Identify the preparation type.
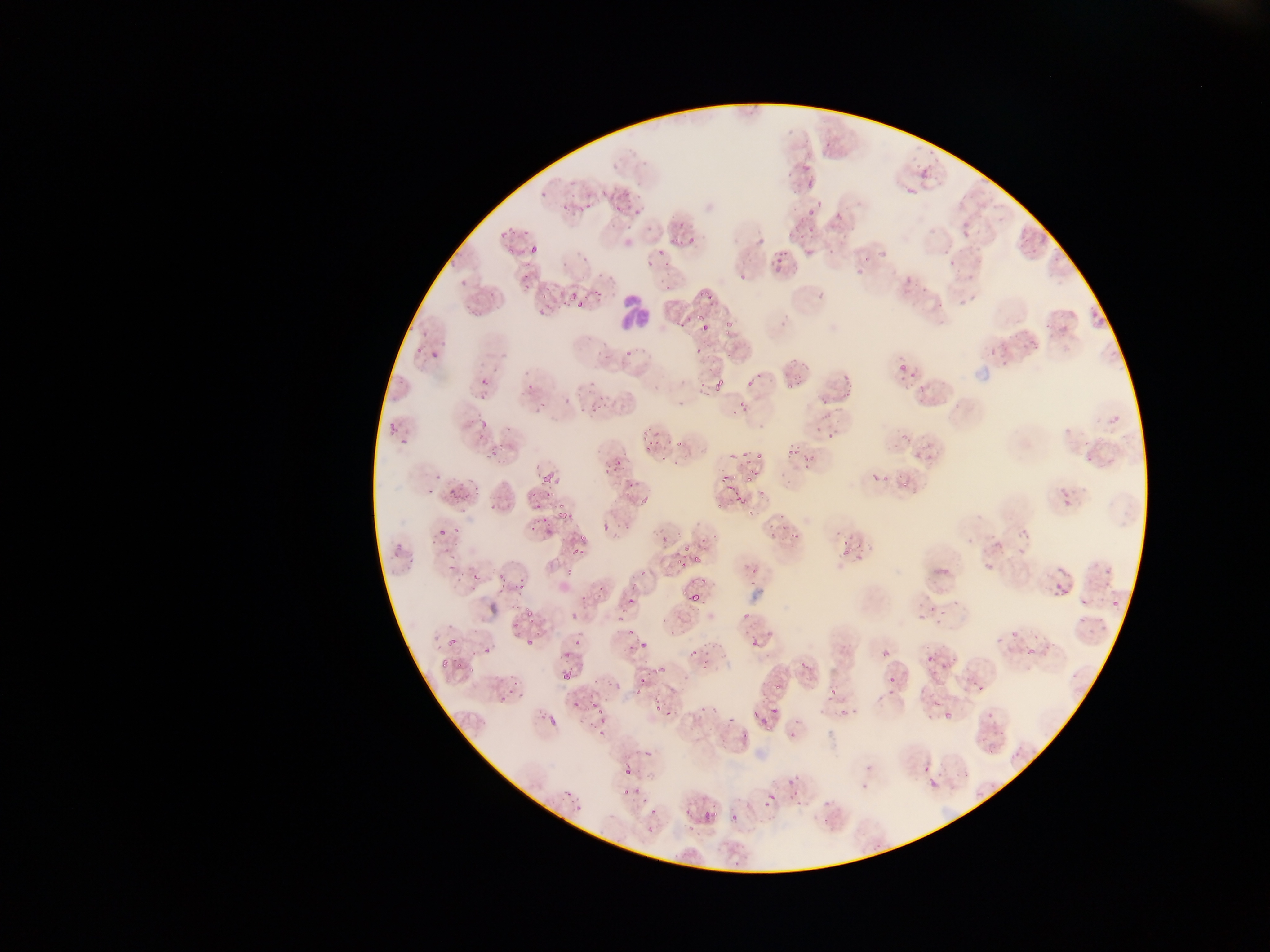
Thin blood smear.

field_of_view: single
leukocyte_locations: 'approximate bounding boxes as {left, top, right, bottom} in pixels: {611, 271, 653, 331}'
image_size: 1270×952 pixels
country: Ghana
malaria_parasite_locations: 'approximate bounding boxes as {left, top, right, bottom} in pixels: {786, 118, 800, 136}, {798, 144, 818, 163}, {913, 145, 932, 162}, {920, 165, 934, 175}, {795, 174, 812, 191}, {908, 183, 918, 193}, {538, 190, 548, 206}, {601, 190, 611, 198}, {611, 192, 641, 217}, {802, 197, 822, 229}, {566, 198, 586, 211}, {504, 216, 521, 241}, {823, 216, 852, 241}, {665, 222, 682, 245}, {957, 225, 971, 239}, {785, 227, 804, 239}, {680, 234, 689, 244}, {620, 235, 631, 249}, {524, 239, 541, 254}, {748, 239, 762, 253}, {859, 244, 882, 269}, {645, 245, 668, 260}, {771, 245, 788, 272}, {505, 247, 517, 258}, {945, 256, 955, 270}, {734, 267, 749, 282}, {514, 269, 535, 289}, {957, 272, 974, 283}, {903, 273, 913, 290}, {455, 279, 472, 290}, {697, 285, 712, 298}, {537, 288, 558, 312}, {957, 289, 984, 312}, {812, 291, 832, 307}, {566, 292, 592, 306}, {462, 302, 483, 324}, {719, 305, 737, 330}, {1084, 311, 1105, 331}, {672, 313, 689, 331}, {700, 322, 710, 333}, {404, 331, 438, 358}, {1022, 335, 1037, 349}, {588, 337, 611, 362}, {689, 341, 705, 358}, {621, 343, 642, 358}, {982, 343, 1002, 354}, {426, 345, 447, 362}, {787, 355, 800, 366}, {999, 360, 1009, 371}, {899, 362, 922, 381}, {744, 365, 763, 392}, {838, 366, 856, 397}, {787, 373, 799, 392}, {476, 375, 502, 398}, {516, 377, 536, 397}, {709, 382, 724, 393}, {584, 387, 612, 416}, {826, 391, 843, 407}, {677, 393, 699, 408}, {732, 397, 750, 416}, {533, 398, 553, 415}, {474, 408, 492, 429}, {1110, 411, 1122, 422}, {385, 419, 401, 441}, {818, 420, 844, 441}, {896, 428, 906, 445}, {642, 430, 661, 453}, {670, 438, 681, 456}, {913, 443, 934, 458}, {488, 446, 496, 455}, {788, 446, 797, 456}, {748, 453, 763, 462}, {800, 454, 813, 469}, {1084, 454, 1097, 469}, {605, 459, 623, 479}, {432, 464, 445, 482}, {541, 468, 556, 486}, {867, 470, 882, 488}, {721, 472, 732, 489}, {457, 475, 483, 500}, {746, 475, 759, 486}, {624, 476, 641, 489}, {884, 476, 889, 486}, {900, 477, 906, 485}, {1059, 481, 1077, 513}, {425, 484, 435, 497}, {444, 489, 455, 503}, {736, 491, 746, 503}, {487, 492, 506, 517}, {635, 495, 651, 508}, {715, 501, 725, 512}, {556, 504, 568, 518}, {532, 505, 550, 530}, {744, 507, 757, 518}, {435, 516, 457, 545}, {602, 517, 615, 536}, {784, 519, 800, 533}, {963, 528, 982, 543}, {1017, 528, 1034, 555}, {654, 530, 675, 555}, {699, 531, 710, 542}, {716, 532, 722, 543}, {841, 533, 859, 559}, {579, 534, 586, 544}, {389, 541, 410, 562}, {567, 545, 574, 555}, {674, 552, 685, 571}, {692, 555, 700, 564}, {448, 557, 462, 578}, {979, 557, 996, 578}, {743, 558, 762, 579}, {1102, 563, 1114, 580}, {560, 564, 578, 581}, {932, 564, 950, 582}, {638, 568, 649, 582}, {469, 569, 482, 584}, {493, 572, 508, 593}, {1049, 575, 1069, 599}, {511, 579, 527, 597}, {1076, 583, 1098, 609}, {591, 584, 605, 599}, {628, 589, 635, 604}, {689, 593, 697, 601}, {1111, 595, 1124, 608}, {920, 605, 933, 618}, {525, 606, 532, 619}, {554, 607, 581, 621}, {615, 607, 630, 618}, {937, 610, 953, 627}, {661, 611, 675, 628}, {1073, 612, 1093, 630}, {743, 614, 751, 623}, {510, 623, 521, 634}, {1008, 623, 1021, 638}, {574, 625, 581, 648}, {623, 625, 634, 642}, {668, 625, 682, 640}, {1087, 626, 1104, 637}, {441, 627, 459, 648}, {1021, 634, 1043, 665}, {744, 635, 762, 649}, {522, 636, 535, 647}, {640, 639, 653, 653}, {483, 642, 498, 656}, {685, 644, 700, 659}, {925, 645, 943, 670}, {557, 648, 572, 665}, {882, 650, 890, 658}, {439, 655, 452, 668}, {795, 657, 808, 677}, {463, 660, 479, 673}, {691, 660, 711, 676}, {640, 669, 666, 691}, {562, 670, 571, 680}, {965, 671, 989, 690}, {1069, 671, 1079, 682}, {771, 676, 782, 696}, {820, 676, 847, 711}, {888, 676, 897, 685}, {496, 686, 513, 704}, {651, 698, 664, 717}, {698, 702, 713, 721}, {767, 702, 786, 713}, {591, 707, 609, 734}, {942, 707, 960, 728}, {724, 709, 734, 723}, {749, 710, 759, 721}, {542, 712, 555, 724}, {978, 712, 997, 724}, {547, 715, 557, 727}, {789, 715, 808, 741}, {758, 719, 776, 733}, {986, 732, 1004, 755}, {622, 765, 645, 783}, {923, 767, 938, 785}, {779, 768, 806, 790}, {857, 769, 871, 790}, {614, 787, 637, 810}, {563, 790, 572, 799}, {785, 791, 806, 806}, {819, 794, 830, 809}, {640, 797, 653, 807}, {763, 797, 774, 812}, {681, 801, 695, 819}, {569, 802, 584, 813}, {706, 806, 718, 824}, {648, 809, 661, 818}, {730, 813, 738, 822}, {645, 825, 658, 839}, {733, 858, 741, 867} | approximate {x, y} pixel centers of objects too small to bound: {939, 301}, {743, 454}, {669, 712}'
capture: mobile-phone photograph through a microscope